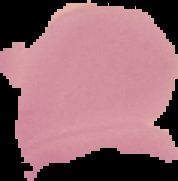
Summary:
  - Image size: 178×181 pixels
  - Image type: segmented cell region on a black background
  - Result: no malaria parasites seen
  - Preparation: thin blood smear